Report the malaria status of this cell.
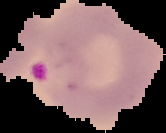
It is parasitized.

image size = 166×133 pixels
preparation = thin blood smear
image type = cell region segmented out of the field of view; surrounding area masked to black